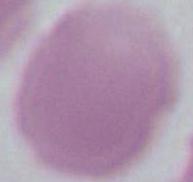
identification = erythrocyte
magnification = 1000x
modality = micrograph